Point out each malaria parasite.
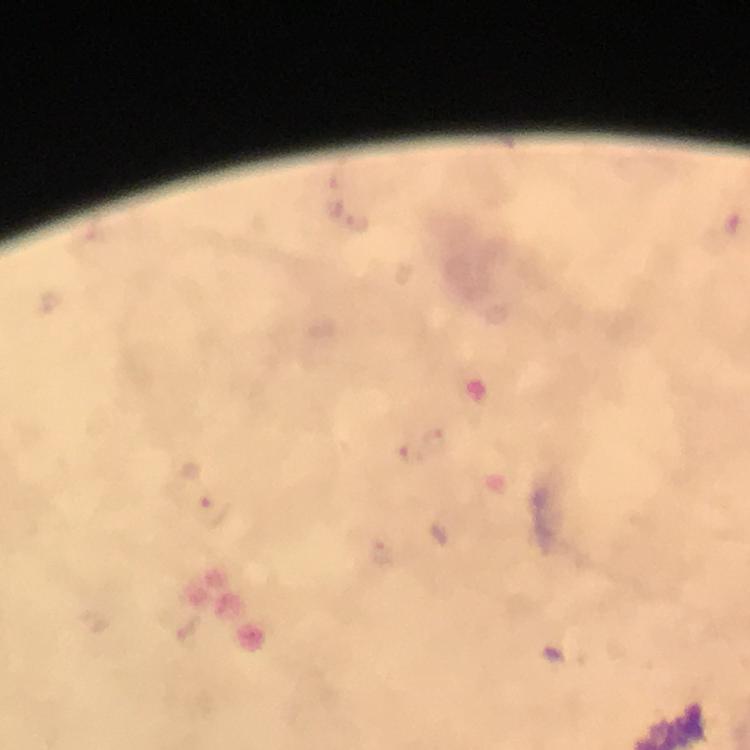

Approximate object centers, in pixels from the top-left corner.
Malaria parasites: (x=410, y=454), (x=216, y=508).

Summary:
  - Immersion oil: used
  - Stain: Giemsa
  - Cropped from: a single field of view
  - Context: from a malaria diagnostic workup
  - Magnification: 100x
  - Capture: smartphone photograph through a microscope
  - Preparation: thick blood film
  - Image size: 750×750 pixels